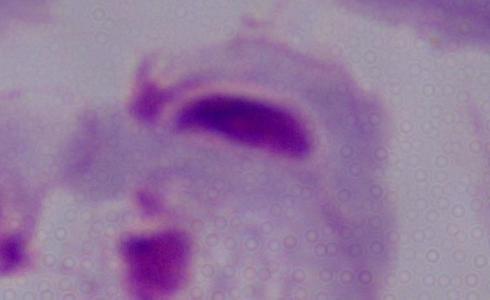
Summary:
  - Magnification: 1000x
  - Modality: photomicrograph
  - Identification: trichomonad